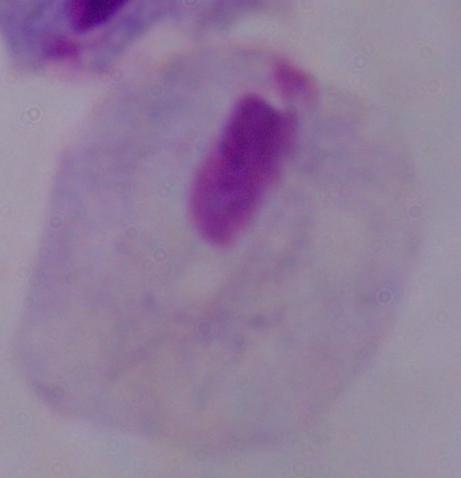
Captured at 1000x magnification. Photomicrograph. A trichomonad is seen.